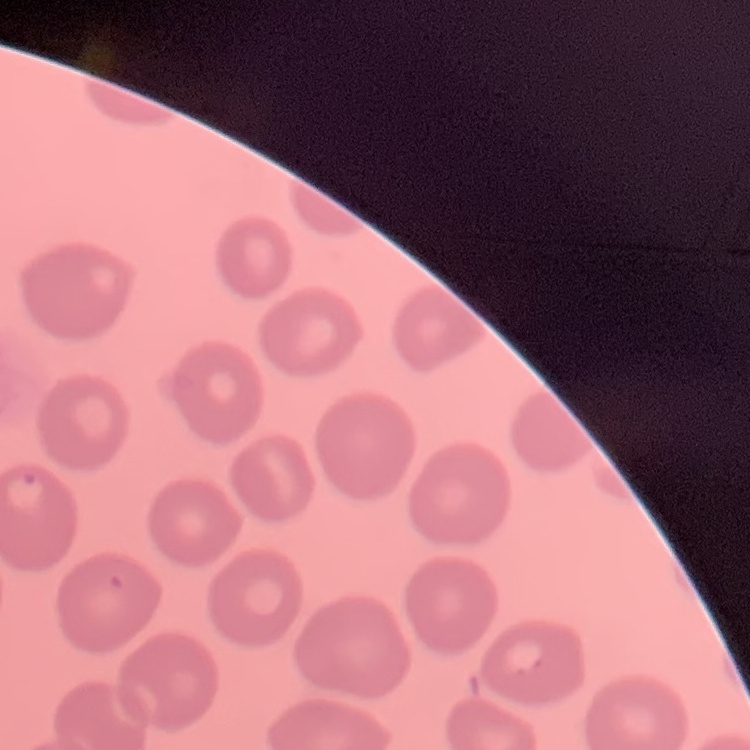 The erythrocytes exhibit no rouleaux formation. Square crop of a larger photomicrograph. Thin peripheral smear. Stained with either Field's or Giemsa.